Assess the morphology of the erythrocytes.
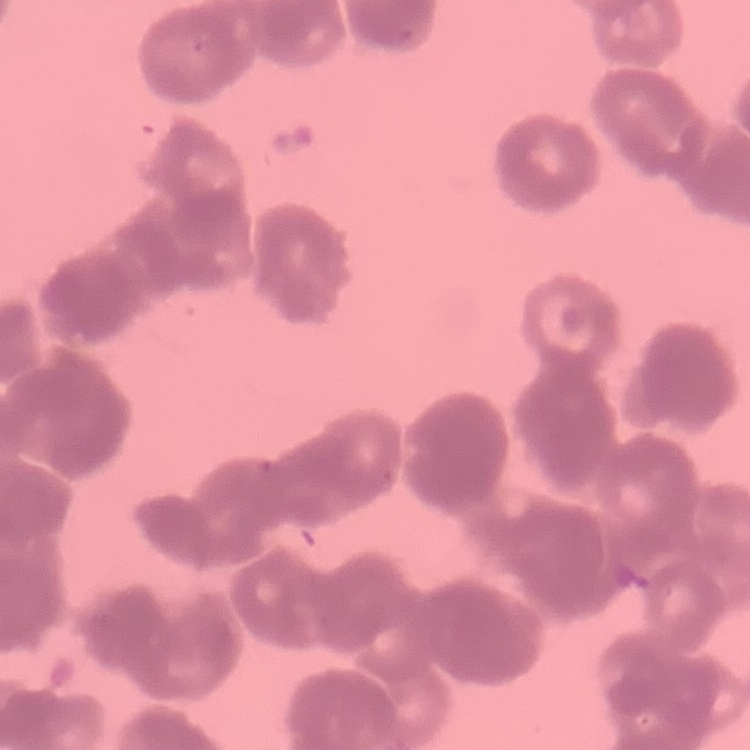

Rouleaux formation.

Square crop of a larger photomicrograph. Thin blood film. Field's or Giemsa stain.